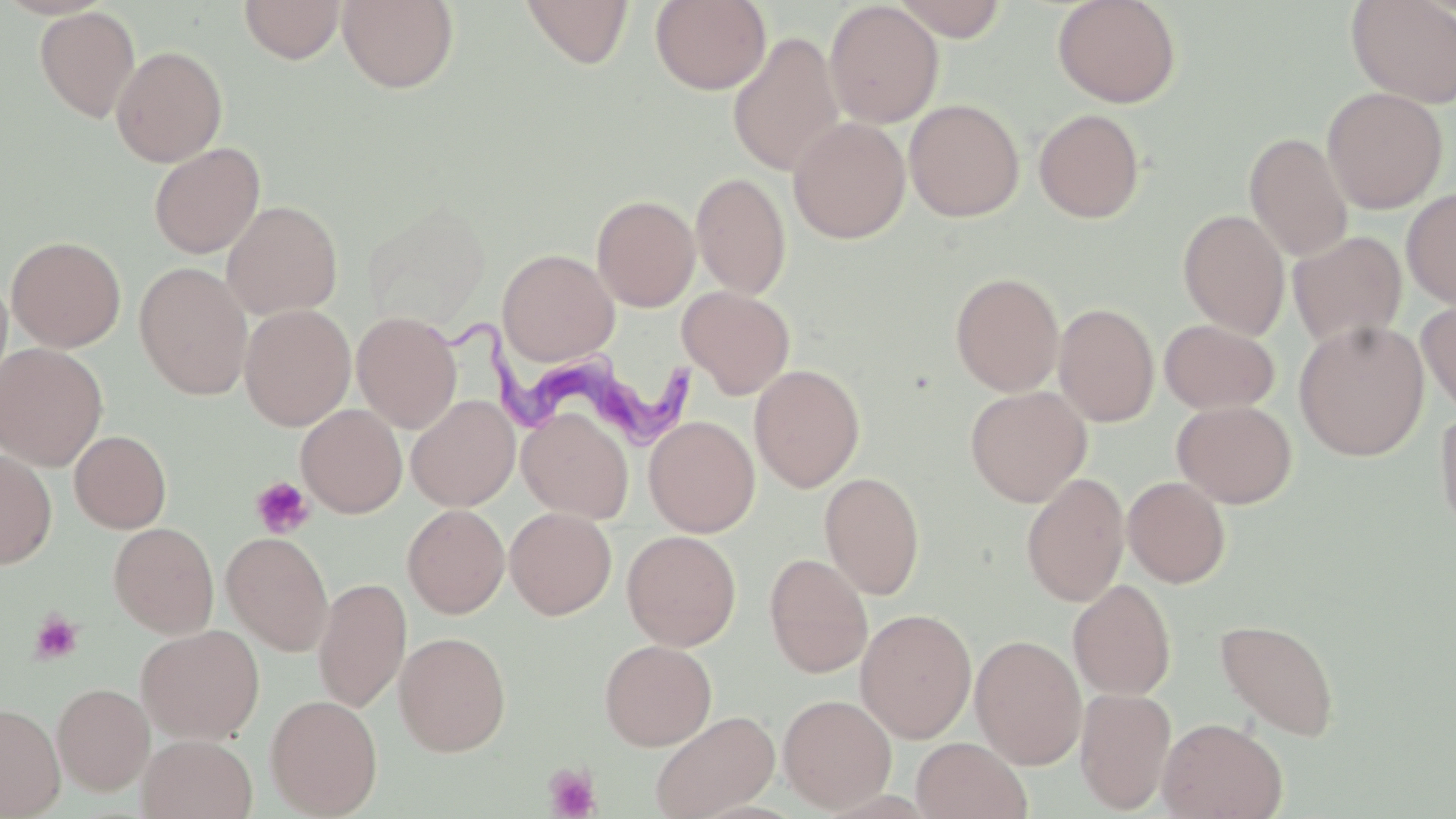
slide_level_diagnosis: Trypanosoma brucei
uninfected_red_blood_cell_locations: 'approximate bounding boxes as [x1, y1, x2, y2] in pixels: [238, 0, 346, 64], [520, 0, 635, 69], [892, 0, 1010, 41], [1051, 0, 1182, 108], [1346, 0, 1456, 109], [337, 1, 459, 93], [650, 1, 772, 95], [824, 1, 944, 128], [35, 6, 141, 123], [727, 31, 846, 177], [111, 45, 228, 167], [1321, 87, 1448, 214], [904, 98, 1025, 222], [1033, 108, 1145, 223], [789, 116, 910, 243], [1244, 132, 1353, 262], [148, 142, 265, 259], [691, 171, 791, 299], [1401, 187, 1456, 308], [591, 194, 700, 312], [222, 200, 343, 319], [1178, 209, 1290, 338], [1288, 231, 1407, 348], [6, 236, 126, 352], [498, 249, 619, 365], [134, 263, 253, 400], [950, 272, 1065, 396], [677, 286, 795, 399], [1416, 297, 1456, 416], [1054, 302, 1159, 427], [239, 304, 356, 431], [352, 311, 462, 433], [1159, 319, 1279, 414], [1293, 319, 1430, 460], [0, 343, 108, 471], [749, 363, 865, 492], [965, 386, 1092, 507], [406, 395, 520, 511], [1172, 400, 1297, 508], [1435, 403, 1456, 542], [296, 404, 407, 518], [517, 407, 634, 523], [643, 416, 760, 537], [69, 430, 172, 533], [0, 448, 57, 569], [1021, 471, 1131, 607], [819, 472, 925, 599], [1122, 476, 1231, 587], [402, 503, 510, 619], [505, 507, 617, 620], [109, 522, 218, 638], [622, 529, 742, 651], [221, 531, 334, 655], [765, 552, 873, 678], [313, 577, 412, 713], [1068, 579, 1177, 700], [855, 608, 977, 743], [1215, 618, 1340, 741], [136, 624, 265, 743], [393, 631, 511, 756], [970, 634, 1087, 769], [599, 639, 717, 751], [52, 682, 154, 795], [1074, 687, 1177, 814], [778, 693, 897, 812], [265, 694, 383, 817], [0, 701, 66, 818], [650, 709, 780, 819], [1157, 717, 1287, 819], [138, 734, 257, 819], [911, 737, 1032, 819]'
trypanosoma_brucei_locations: 'approximate bounding boxes as [x1, y1, x2, y2] in pixels: [430, 314, 702, 448]'
field_of_view: one of a larger specimen
platelet_locations: 'approximate bounding boxes as [x1, y1, x2, y2] in pixels: [250, 477, 315, 539], [29, 611, 84, 664], [544, 763, 602, 819]'
magnification: 1000x
stain: May-Grünwald-Giemsa
image_size: 1456×819 pixels
preparation: thin blood smear
modality: optical microscopy